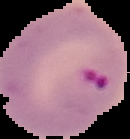

From a thin blood film. Result: Plasmodium parasites identified. Image is 130×139 pixels. Cell region segmented out of the field of view; the surrounding area is masked to black.